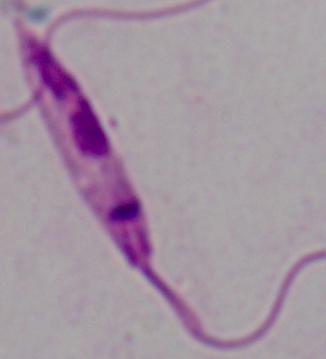
{
  "identification": "Leishmania",
  "magnification": "1000x",
  "modality": "micrograph"
}